Report the malaria status of this cell.
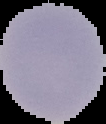

It is uninfected.

Image is 106×124 pixels. From a thin blood smear. Segmented cell region on a black background.